Report the malaria status of this cell.
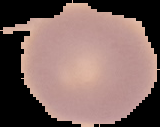

Uninfected.

The area outside the segmented cell region is set to black. Image is 160×127 pixels. From a thin blood film.